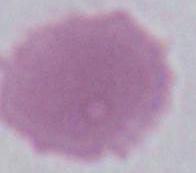 Photomicrograph. Captured at 1000x magnification. An erythrocyte is seen.